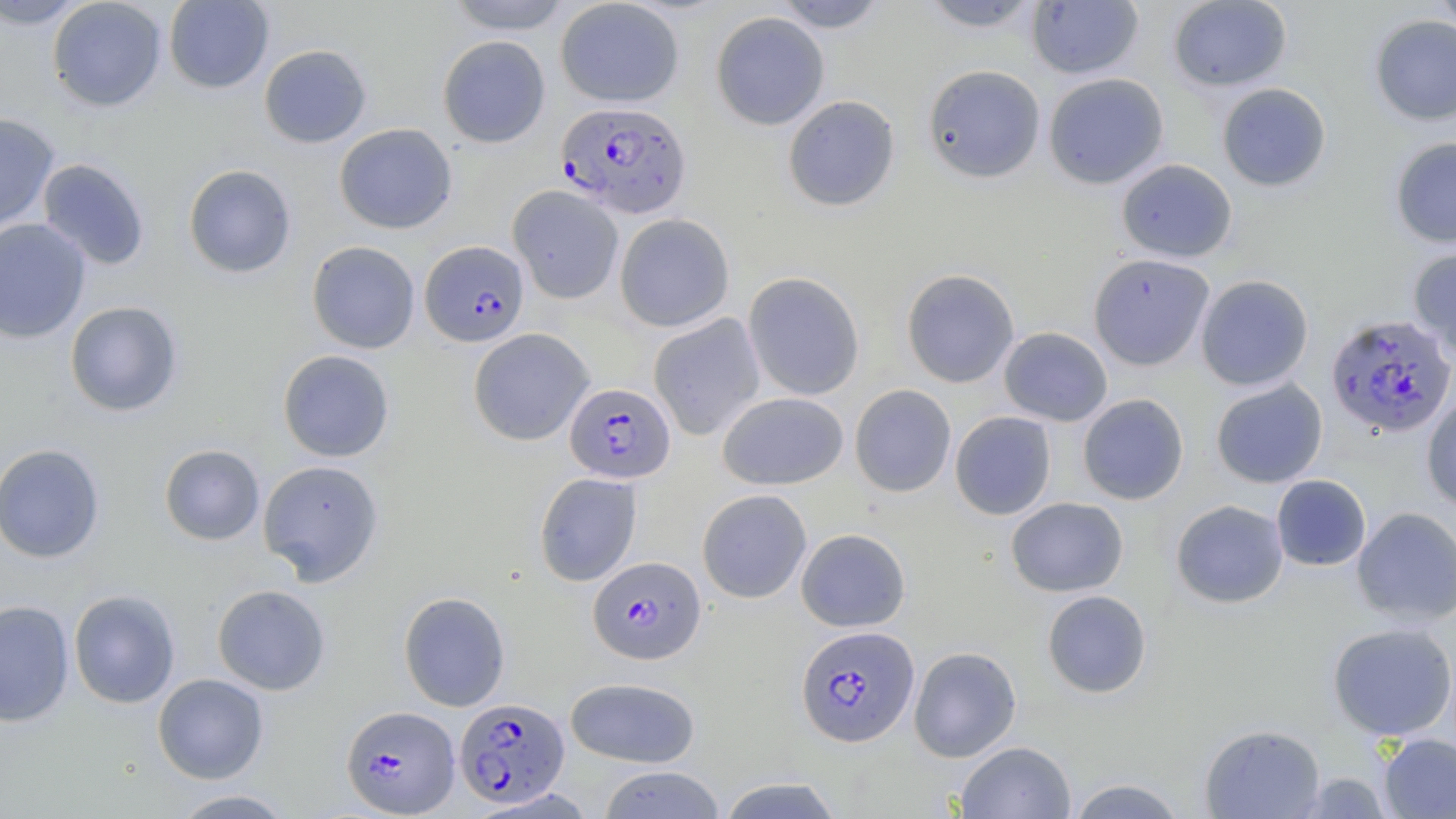

slide-level diagnosis = Plasmodium falciparum
magnification = 1000x
Plasmodium falciparum-infected red blood cell locations = approximate bounding boxes as (x1,y1)-(x2,y2) corner pairs in pixels: (556,101)-(691,218), (420,240)-(529,346), (1325,313)-(1456,439), (564,382)-(676,483), (588,556)-(705,665), (795,624)-(919,747), (454,697)-(570,808), (341,705)-(460,816)
field of view = single
modality = light microscopy
uninfected red blood cell locations = approximate bounding boxes as (x1,y1)-(x2,y2) corner pairs in pixels: (0,0)-(91,28), (47,0)-(167,111), (164,0)-(274,93), (444,0)-(575,34), (555,0)-(684,107), (771,0)-(891,32), (1168,0)-(1292,92), (1430,0)-(1456,35), (916,1)-(1045,32), (1027,1)-(1144,79), (710,11)-(830,131), (1369,15)-(1456,126), (437,35)-(551,148), (258,44)-(372,148), (922,64)-(1046,183), (1043,73)-(1169,189), (1217,83)-(1331,191), (783,94)-(900,212), (0,113)-(60,231), (334,122)-(457,234), (1390,137)-(1456,248), (37,158)-(150,270), (1116,158)-(1237,263), (182,163)-(297,279), (508,185)-(624,304), (614,213)-(735,332), (0,218)-(91,343), (307,240)-(420,354), (1408,248)-(1456,359), (1088,253)-(1215,371), (901,268)-(1020,388), (743,271)-(865,401), (1195,274)-(1314,392), (64,300)-(184,417), (649,314)-(765,440), (468,327)-(594,446), (998,327)-(1113,426), (277,350)-(395,462), (1210,379)-(1328,489), (850,384)-(956,497), (718,392)-(848,490), (1077,394)-(1189,505), (1421,395)-(1456,512), (949,411)-(1057,520), (0,443)-(105,563), (159,444)-(265,545), (258,459)-(384,585), (533,472)-(642,587), (1271,475)-(1371,571), (697,489)-(812,603), (1006,497)-(1128,597), (1170,499)-(1289,608), (1351,506)-(1456,626), (796,528)-(911,632), (212,584)-(330,695), (68,589)-(181,709), (1041,590)-(1152,698), (398,591)-(511,712), (0,599)-(75,727), (1327,622)-(1456,740), (908,646)-(1022,762), (152,673)-(269,783), (565,677)-(700,768), (1200,723)-(1326,818), (1378,733)-(1456,818), (955,740)-(1075,819), (598,766)-(726,818), (1294,772)-(1394,818), (716,775)-(846,819), (1066,777)-(1189,818), (168,789)-(297,818)
preparation = thin blood smear
stain = May-Grünwald-Giemsa
image size = 1456×819 pixels